Locate every uninfected red blood cell.
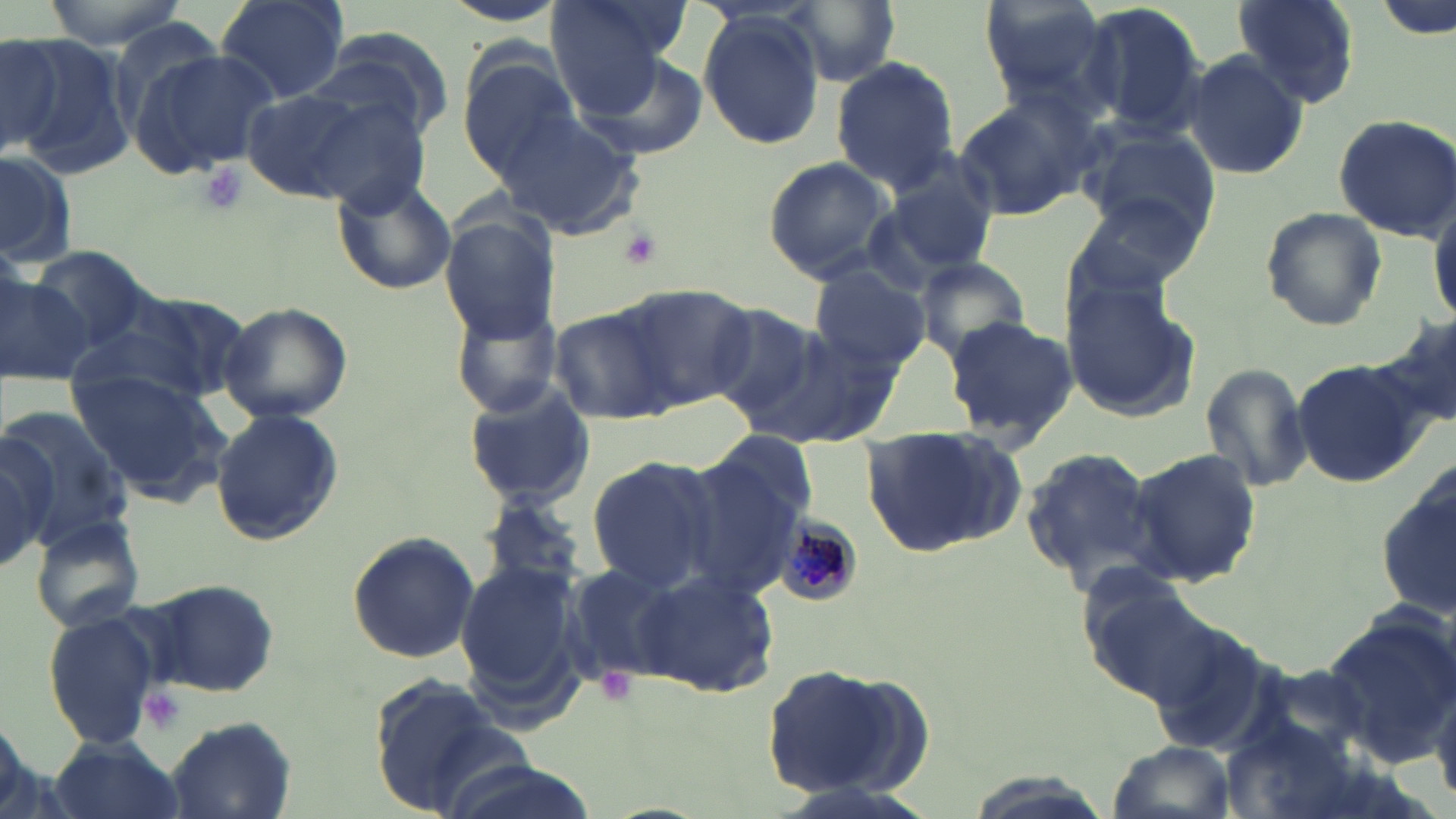
Approximate bounding boxes as (x1, y1, x2, y2) in pixels.
Uninfected red blood cells: (38, 0, 198, 51), (217, 0, 351, 103), (548, 0, 674, 117), (976, 0, 1115, 105), (1232, 0, 1362, 108), (782, 1, 904, 85), (438, 2, 570, 29), (1080, 2, 1209, 140), (697, 13, 825, 149), (0, 31, 65, 156), (299, 34, 449, 147), (6, 35, 132, 175), (127, 44, 280, 178), (580, 50, 708, 161), (1181, 51, 1311, 179), (459, 57, 578, 174), (829, 58, 958, 189), (239, 88, 376, 203), (951, 91, 1097, 222), (310, 101, 432, 217), (497, 109, 647, 240), (1330, 113, 1456, 242), (1077, 125, 1220, 241), (0, 150, 77, 266), (881, 150, 1000, 277), (762, 156, 897, 284), (331, 175, 458, 295), (1428, 192, 1456, 329), (1070, 194, 1204, 303), (1258, 205, 1388, 331), (440, 211, 560, 341), (27, 248, 151, 355), (915, 257, 1031, 363), (810, 266, 931, 375), (1, 276, 95, 385), (1060, 278, 1201, 422), (613, 283, 758, 409), (80, 289, 241, 409), (448, 296, 563, 419), (218, 301, 353, 423), (550, 306, 679, 424), (705, 307, 822, 420), (942, 314, 1079, 447), (755, 322, 899, 448), (1290, 356, 1429, 489), (1201, 360, 1316, 495), (69, 369, 228, 499), (461, 383, 595, 508), (1, 405, 129, 550), (207, 408, 344, 546), (860, 424, 1023, 561), (0, 435, 56, 570), (683, 435, 815, 590), (1018, 443, 1166, 593), (1125, 446, 1261, 588), (584, 455, 718, 592), (1377, 466, 1456, 619), (480, 495, 590, 596), (27, 514, 147, 634), (344, 530, 480, 663), (556, 558, 682, 687), (455, 560, 580, 706), (638, 572, 779, 698), (1078, 577, 1222, 708), (146, 578, 280, 696), (44, 611, 161, 750), (1317, 614, 1456, 765), (1146, 623, 1275, 759), (757, 663, 916, 798), (365, 677, 525, 815), (1430, 679, 1456, 810), (163, 713, 295, 818), (1224, 718, 1369, 819), (46, 737, 186, 818), (1103, 739, 1239, 819), (430, 758, 603, 819).

Summary:
  - Plasmodium malariae-infected red blood cell locations: (776, 519, 862, 607)
  - Platelet locations: (199, 160, 247, 214), (618, 226, 663, 270), (596, 667, 638, 706), (139, 685, 188, 737)
  - Slide-level diagnosis: Plasmodium malariae
  - Stain: May-Grünwald-Giemsa
  - Magnification: 1000x
  - Field of view: single
  - Image size: 1456×819 pixels
  - Preparation: thin blood smear
  - Modality: optical microscopy